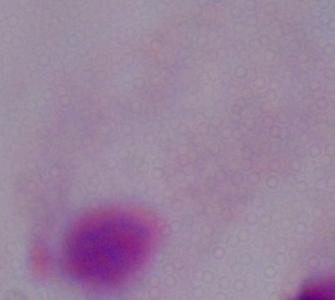
Summary:
  - Magnification: 1000x
  - Modality: micrograph
  - Identification: trichomonad